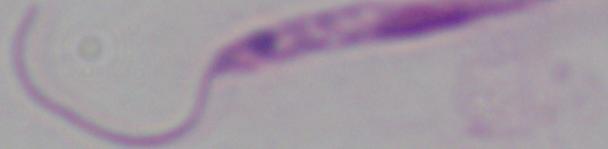

Captured at 1000x magnification. A Leishmania parasite is shown. Photomicrograph.